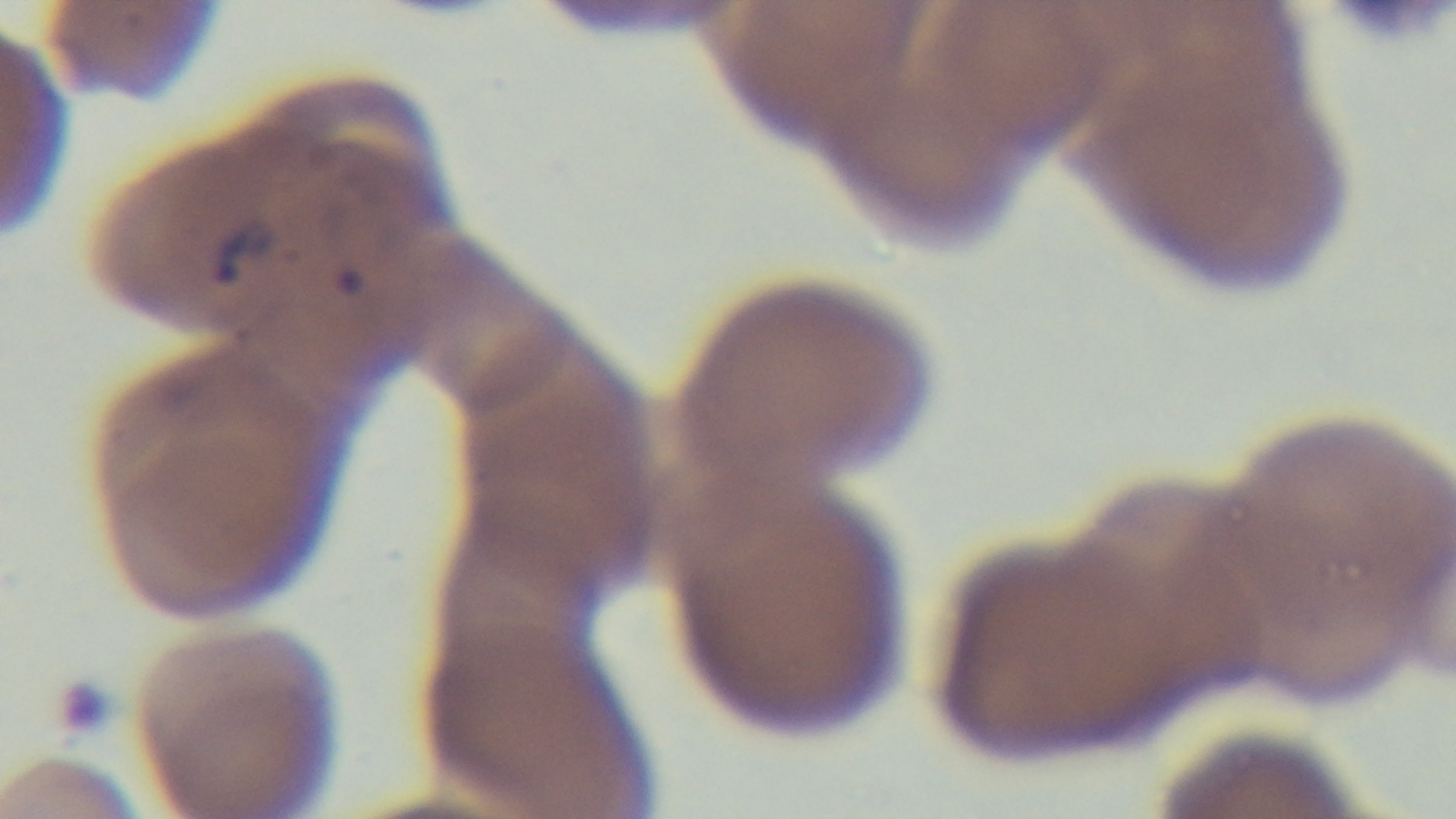

Malaria status: positive. Single field of view. Light microscopy. Preparation: thin. Captured with a mounted 4K digital camera. Giemsa stain. Oil-immersion objective, 100x.